Name the parasite shown.
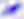

This is Toxoplasma gondii.

Captured at 400x magnification. Micrograph.